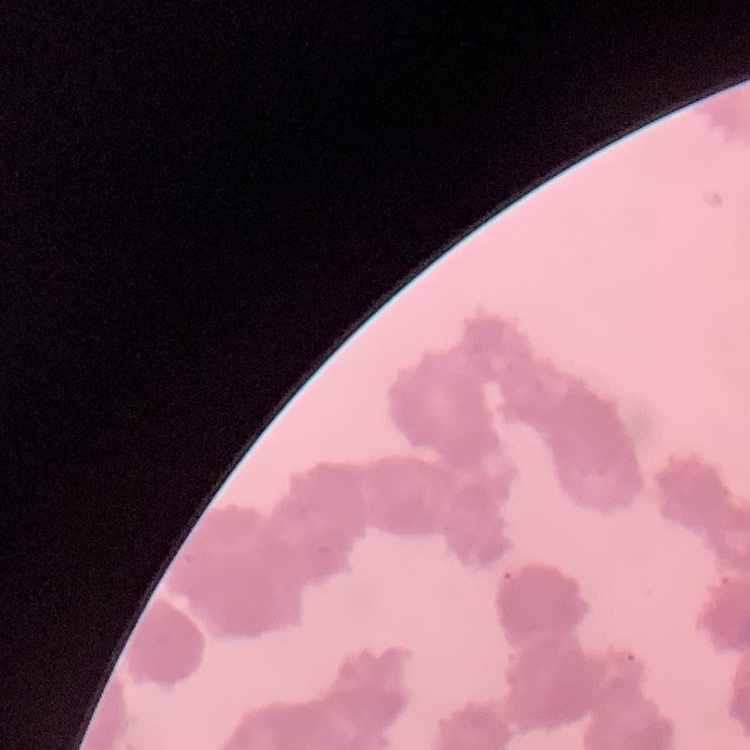
erythrocyte morphology = rouleaux formation
preparation = thin peripheral smear
image type = square crop of a larger photomicrograph
stain = Field's or Giemsa